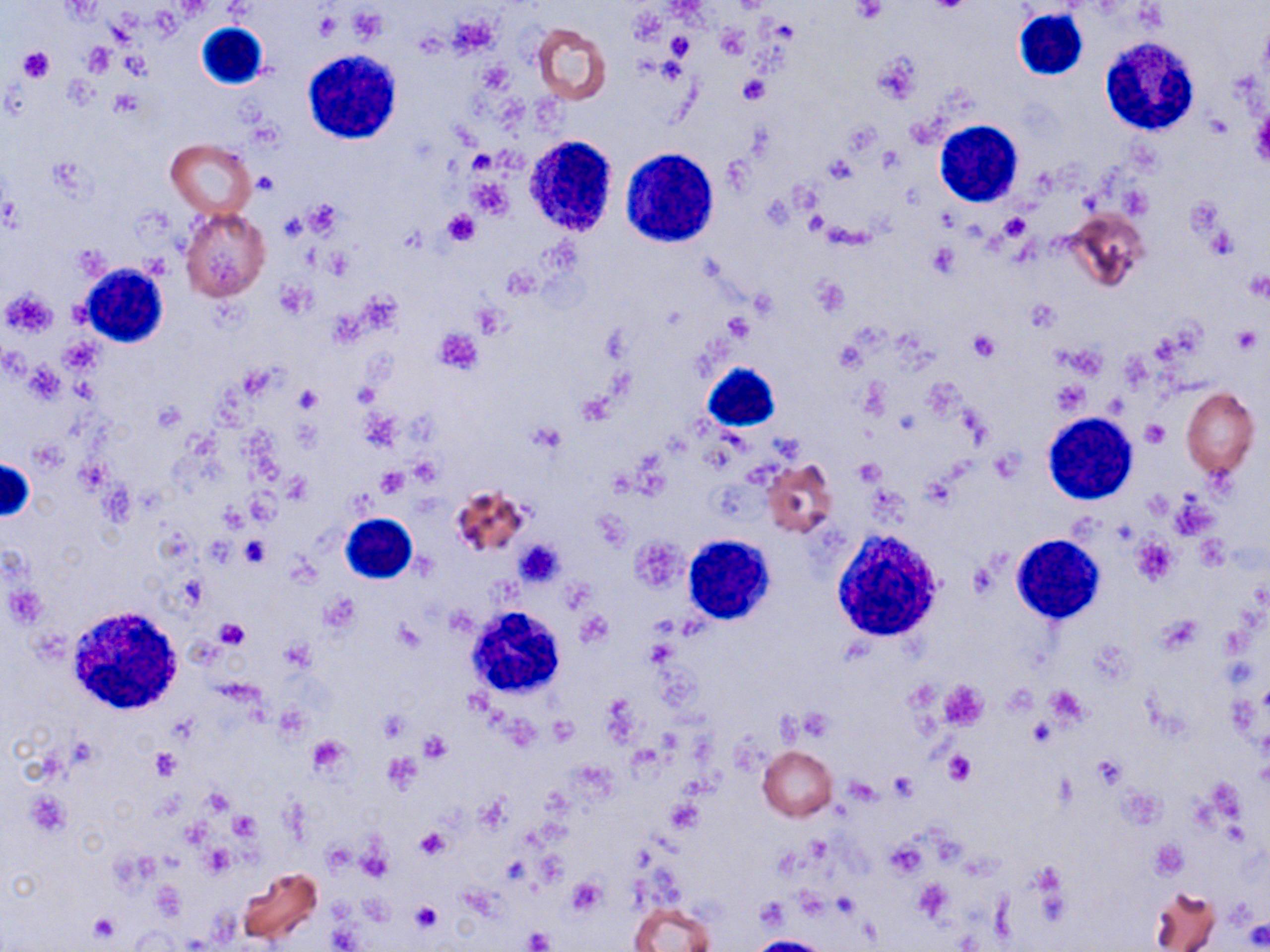

slide-level diagnosis = no evidence of blood parasites
image size = 1270×952 pixels
white blood cell locations = approximate bounding boxes as [x1, y1, x2, y2] in pixels: [1013, 8, 1087, 83], [197, 22, 269, 89], [1097, 38, 1200, 136], [302, 48, 403, 144], [934, 120, 1024, 207], [524, 137, 619, 238], [621, 147, 721, 245], [79, 264, 168, 348], [701, 361, 781, 432], [1043, 411, 1137, 505], [1, 457, 34, 521], [341, 514, 417, 586], [833, 528, 945, 641], [683, 534, 774, 625], [1011, 534, 1104, 624], [68, 605, 184, 714], [463, 605, 568, 700]
field of view = one of a larger specimen
preparation = thin blood film
platelet locations = approximate bounding boxes as [x1, y1, x2, y2] in pixels: [923, 1, 976, 14], [852, 2, 886, 23], [349, 7, 388, 42], [313, 12, 341, 39], [667, 32, 693, 58], [83, 43, 115, 75], [18, 46, 54, 83], [872, 53, 919, 104], [740, 75, 769, 104], [1249, 106, 1270, 170], [469, 149, 498, 173], [254, 171, 276, 195], [466, 178, 513, 220], [302, 201, 341, 236], [440, 209, 480, 247], [1000, 213, 1033, 241], [927, 244, 960, 278], [811, 276, 850, 317], [1, 288, 57, 338], [1025, 298, 1061, 332], [1231, 325, 1262, 352], [435, 329, 483, 376], [969, 330, 1000, 361], [1051, 381, 1088, 414], [296, 386, 320, 413], [1142, 420, 1168, 446], [528, 423, 564, 453], [375, 468, 409, 496], [239, 537, 270, 567], [1132, 537, 1178, 586], [515, 539, 564, 586], [577, 612, 611, 646], [217, 618, 249, 649], [392, 621, 425, 653], [938, 680, 988, 731], [376, 710, 409, 743], [548, 716, 577, 745], [419, 733, 450, 763], [307, 735, 350, 774], [151, 748, 181, 780], [944, 749, 977, 785], [383, 752, 422, 792], [1091, 757, 1124, 787], [887, 772, 917, 798], [27, 792, 71, 836], [668, 799, 704, 832], [231, 813, 258, 843], [414, 827, 451, 860], [886, 840, 927, 878], [1151, 840, 1187, 879], [202, 845, 236, 876], [565, 876, 607, 916], [913, 878, 953, 920], [410, 901, 442, 932], [88, 911, 122, 944], [328, 926, 359, 950], [524, 927, 553, 950]
magnification = 1000x
stain = May-Grünwald-Giemsa
modality = light microscopy
uninfected red blood cell locations = approximate bounding boxes as [x1, y1, x2, y2] in pixels: [533, 23, 612, 105], [167, 139, 255, 218], [181, 208, 271, 302], [1064, 211, 1148, 292], [1181, 387, 1258, 478], [761, 459, 837, 537], [449, 484, 531, 560], [758, 746, 837, 821], [238, 866, 324, 947], [1149, 885, 1220, 952], [629, 900, 715, 952]